Assess this cell for malaria.
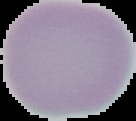

Uninfected.

From a thin blood smear. The area outside the segmented cell region is set to black. Image is 136×121 pixels.